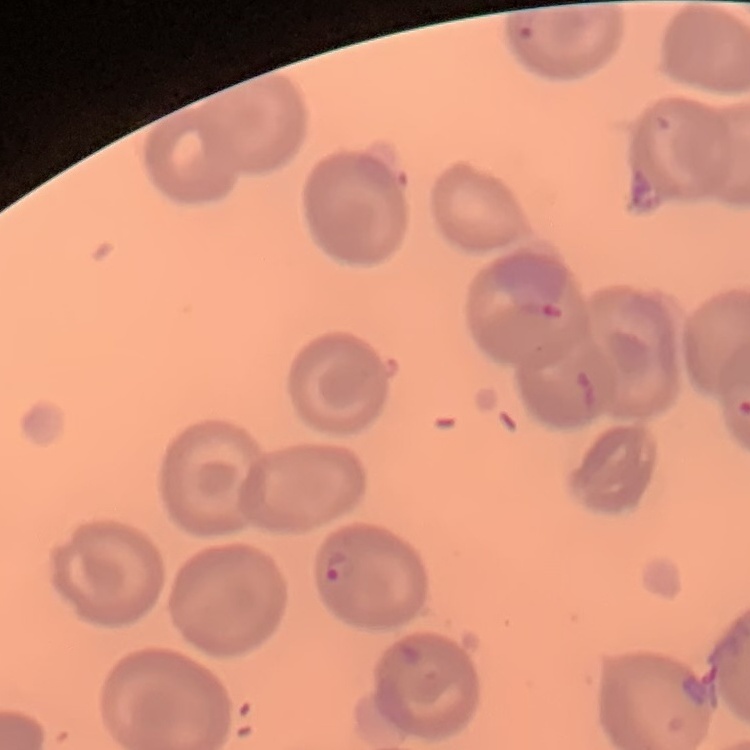

red blood cell morphology = no rouleaux formation
stain = Field's or Giemsa
image type = square crop of a larger photomicrograph
preparation = thin blood film